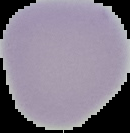
Image is 130×133 pixels. Malaria status: uninfected. From a thin blood smear. Segmented cell region on a black background.